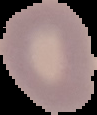

Image is 97×115 pixels. Malaria status: uninfected. From a thin blood film. Cell region segmented out of the field of view; the surrounding area is masked to black.